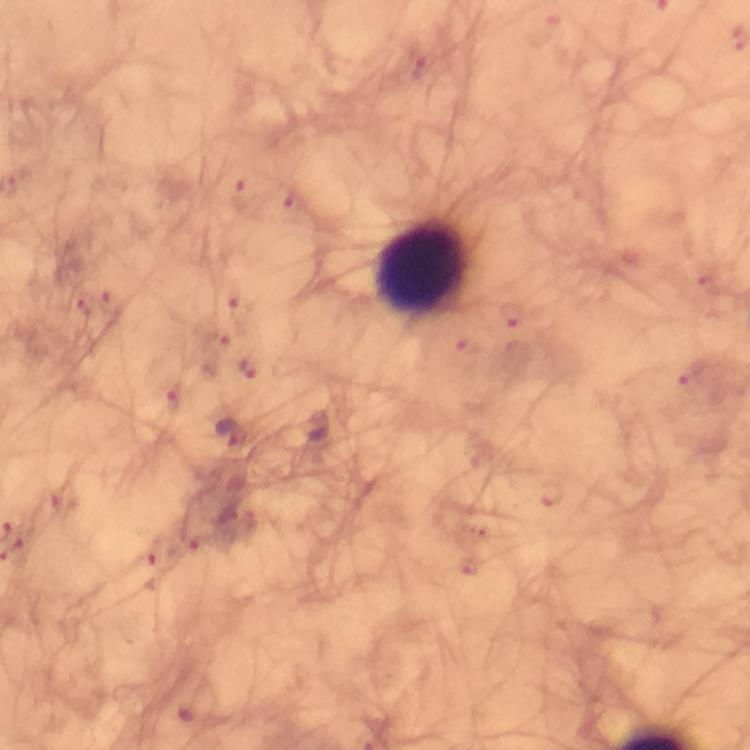

Approximate centers as {x, y} in pixels.
Summary:
  - Plasmodium parasite locations: {229, 436}
  - Leukocyte locations: {423, 265}
  - Image size: 750×750 pixels
  - Context: from a diagnostic examination for malaria
  - Immersion oil: applied
  - Stain: Giemsa
  - Cropped from: one field of view
  - Preparation: thick blood smear
  - Capture: smartphone photograph through a microscope
  - Magnification: 100x